Locate every malaria parasite.
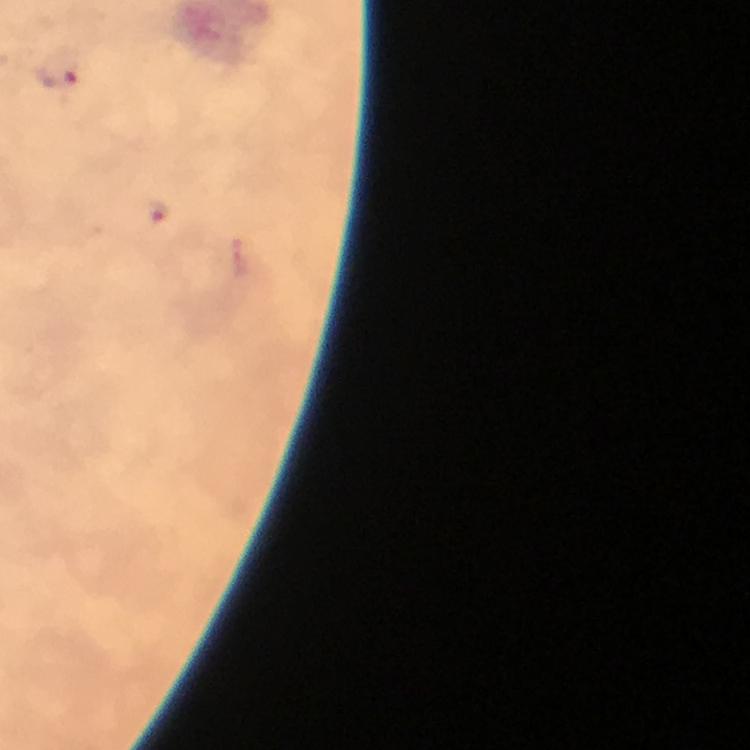
Approximate object centers, in pixels from the top-left corner.
Malaria parasites: (x=58, y=71), (x=156, y=212).

magnification: 100x
context: from a malaria diagnostic workup
immersion_oil: used
cropped_from: one field of view
stain: Giemsa
preparation: thick smear
capture: smartphone photograph through a microscope
image_size: 750×750 pixels